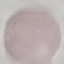

result: negative for malaria parasites
preparation: thin blood film
image_type: automatically extracted cell patch, resized to 64 × 64 pixels
capture: smartphone camera at the microscope eyepiece
stain: Giemsa